Evaluate for malaria.
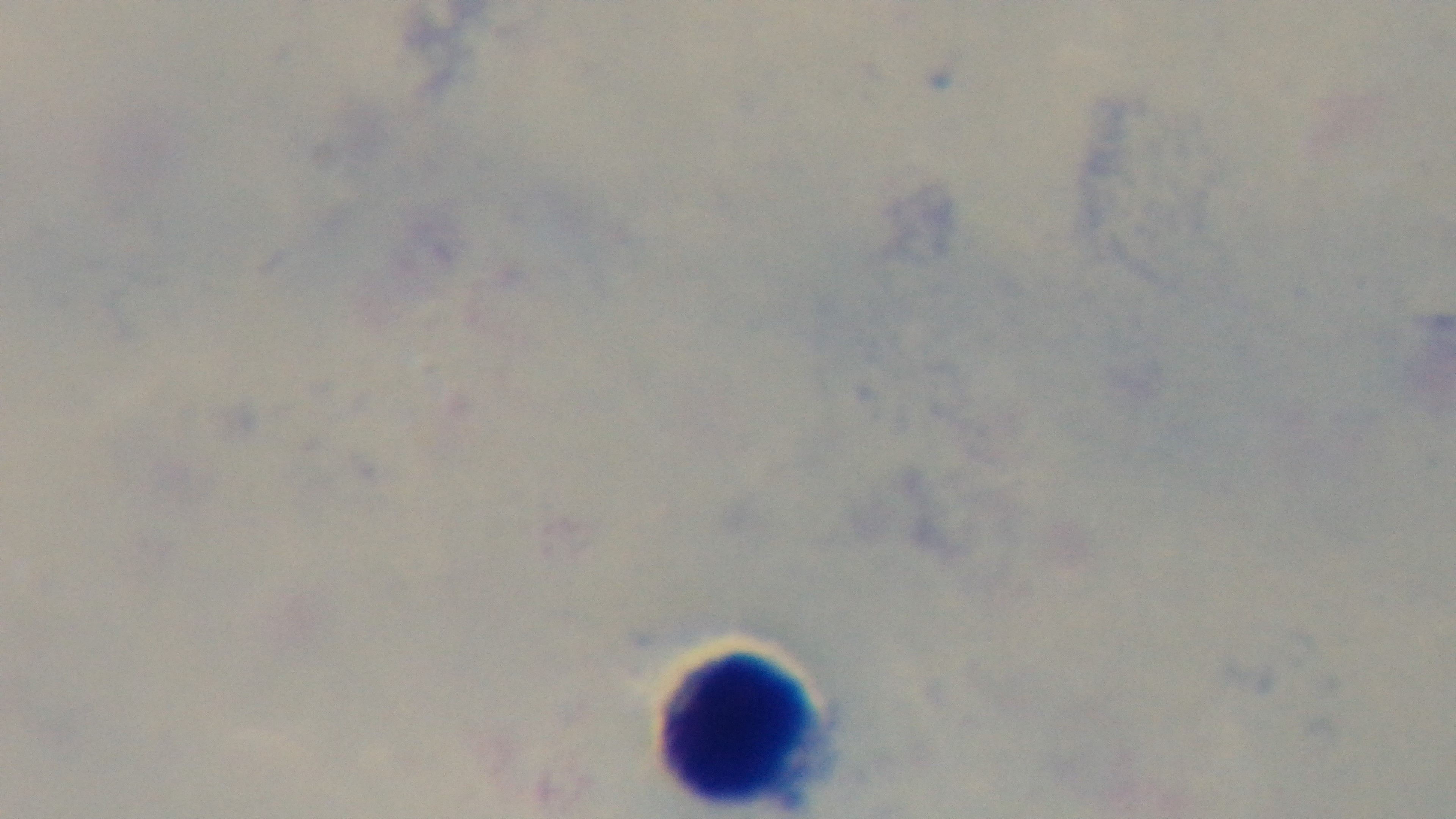

Uninfected.

Light microscopy. 100x oil-immersion objective. Mounted 4K digital camera. One field from the slide. Preparation: thick. Giemsa stain.